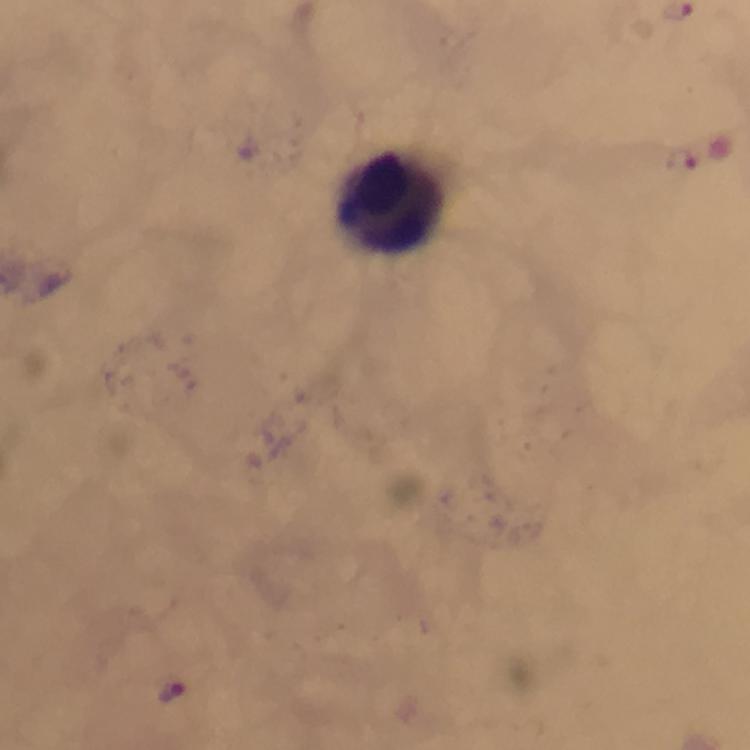
Approximate centers as (x, y) in pixels. Malaria parasite locations: (676, 9), (682, 161), (172, 693). Leukocyte locations: (389, 201). From a malaria diagnostic workup. Smartphone photograph taken through a microscope. Cropped region of a single field of view. Thick blood film. Giemsa stain. At 100x magnification. Immersion oil was used. Image is 750×750 pixels.